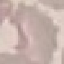
malaria status = uninfected
stain = Giemsa
image type = cell patch, automatically extracted from a larger field of view and resized to 64 × 64 pixels
preparation = thin smear
capture = smartphone through the microscope eyepiece